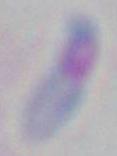

modality: micrograph
magnification: 1000x
identification: Toxoplasma gondii